Describe the morphology of the erythrocytes.
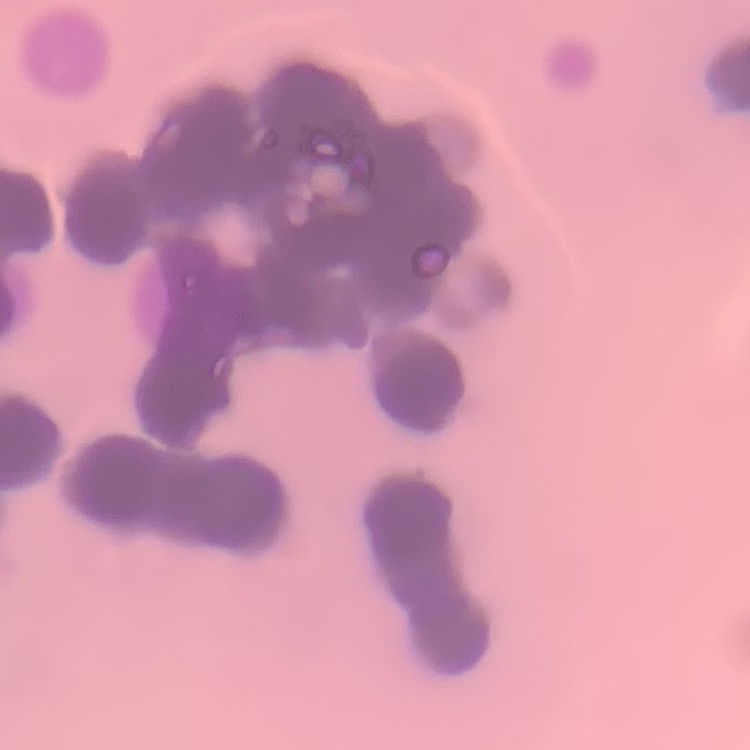
They show rouleaux formation.

preparation = thin blood film
image type = square crop of a larger photomicrograph
stain = Field's or Giemsa